Identify the blood parasite species.
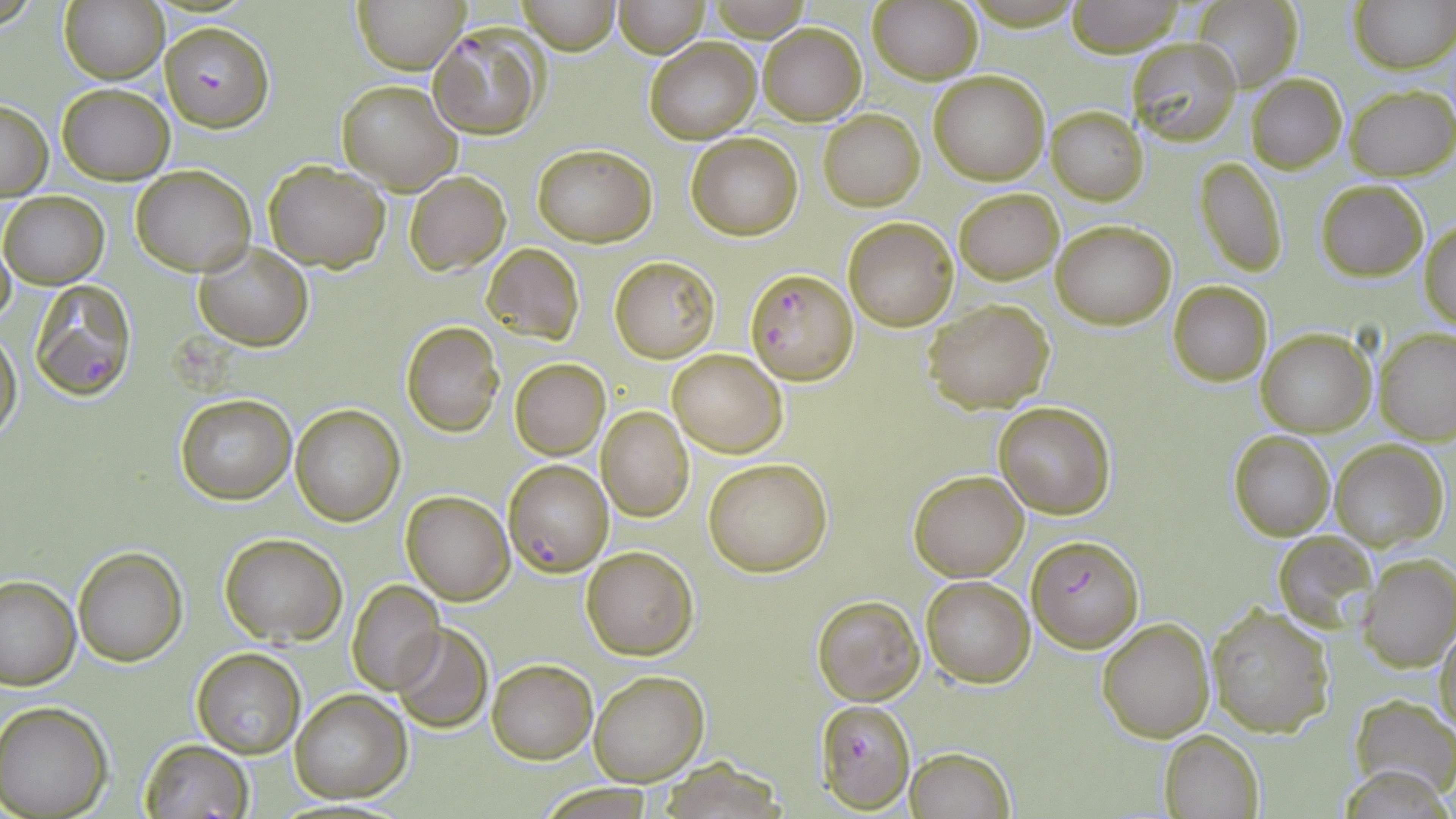

Plasmodium falciparum.

Approximate bounding boxes as (x1,y1)-(x2,y2) corner pairs in pixels. Platelet locations: (174,335)-(242,397). Plasmodium falciparum-infected red blood cell locations: (160,20)-(274,133), (429,23)-(548,140), (744,268)-(858,386), (29,282)-(136,400), (503,459)-(613,577), (1027,534)-(1143,651), (816,700)-(916,811). Uninfected red blood cell locations: (61,0)-(168,84), (355,0)-(467,72), (514,0)-(620,53), (708,0)-(813,41), (1192,0)-(1302,94), (1349,0)-(1455,73), (613,1)-(709,57), (1067,1)-(1184,56), (869,3)-(982,84), (759,24)-(864,125), (644,36)-(760,145), (1125,39)-(1243,148), (928,69)-(1050,185), (1246,74)-(1346,172), (336,79)-(462,195), (56,83)-(174,184), (1347,84)-(1456,181), (1,98)-(52,200), (1046,106)-(1147,205), (819,110)-(925,210), (685,133)-(802,240), (532,144)-(656,247), (1195,156)-(1287,276), (265,159)-(390,272), (131,166)-(255,276), (406,172)-(510,275), (1316,179)-(1427,280), (953,187)-(1064,283), (1,192)-(108,289), (843,215)-(959,331), (1051,219)-(1176,329), (1420,219)-(1455,329), (0,230)-(15,332), (194,241)-(313,350), (482,244)-(584,345), (609,256)-(719,362), (1168,282)-(1272,386), (923,299)-(1055,413), (400,321)-(505,437), (1,324)-(22,451), (1256,327)-(1375,438), (1374,328)-(1456,443), (667,348)-(787,457), (510,359)-(609,458), (175,393)-(296,505), (992,401)-(1115,520), (290,404)-(405,526), (596,404)-(694,521), (1228,431)-(1336,541), (1331,440)-(1447,550), (702,456)-(833,575), (908,470)-(1029,580), (401,492)-(514,605), (1270,530)-(1375,630), (219,533)-(347,645), (72,546)-(186,667), (581,546)-(699,660), (1359,554)-(1455,672), (0,573)-(79,690), (920,574)-(1035,687), (346,579)-(446,695), (811,595)-(924,705), (1205,604)-(1334,738), (1098,616)-(1215,741), (391,622)-(492,733), (1434,623)-(1456,737), (192,649)-(307,759), (487,658)-(596,763), (589,671)-(708,786), (290,689)-(411,804), (1352,694)-(1455,802), (1,702)-(115,819), (1159,730)-(1265,819), (138,740)-(253,819), (905,747)-(1015,819). Single field of view. 1000x magnification. Thin blood film. Image is 1456×819 pixels. May-Grünwald-Giemsa stain. Optical microscopy.